Identify the parasite.
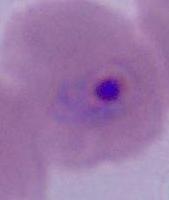

This is Plasmodium.

Photomicrograph. 400x or 1000x magnification.